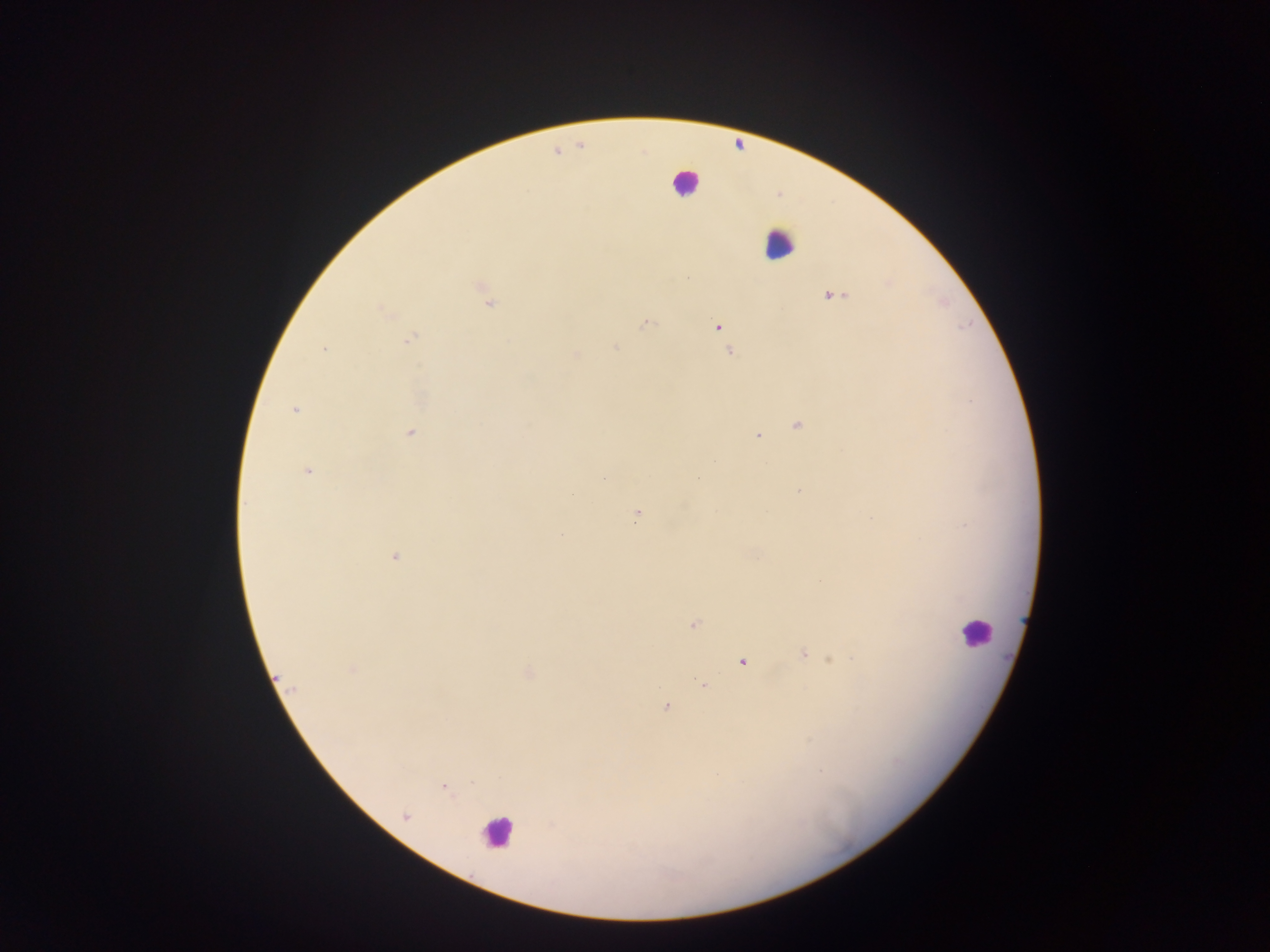

Approximate centers as x y in pixels.
Summary:
  - Leukocyte locations: 685 184; 778 244; 976 632; 496 833
  - Plasmodium parasite locations: 556 151; 481 287; 831 295; 488 303; 383 310; 646 323; 716 326; 722 329; 411 339; 613 346; 323 349; 729 351; 575 355; 295 410; 797 424; 409 432; 758 434; 307 471; 605 477; 799 490; 636 516; 561 535; 394 557; 693 623; 803 653; 831 659; 741 661; 352 670; 527 673; 703 685; 666 706; 444 787; 406 817
  - Capture: mobile-phone photograph through a microscope
  - Field of view: single
  - Image size: 1270×952 pixels
  - Preparation: thick blood film
  - Country: Ghana